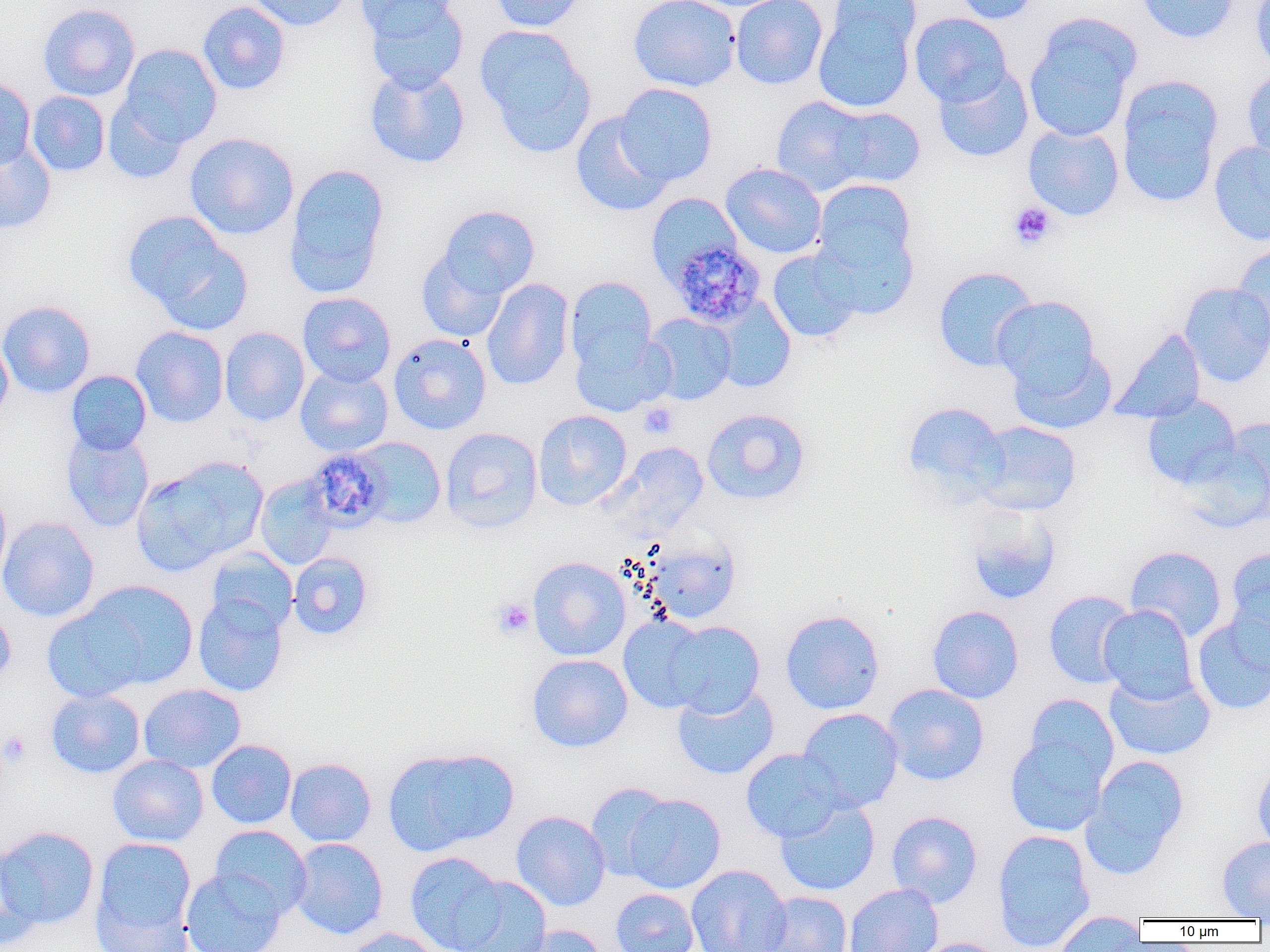

Approximate bounding boxes as (x1, y1, x2, y2) in pixels. Platelet locations: (1008, 202, 1056, 250), (639, 402, 678, 439), (491, 597, 536, 639), (0, 730, 32, 767). Plasmodium malariae-infected red blood cell locations: (668, 240, 766, 328), (303, 447, 391, 533). Uninfected red blood cell locations: (245, 0, 353, 32), (357, 0, 458, 42), (363, 0, 469, 93), (488, 0, 589, 33), (628, 0, 741, 92), (730, 0, 827, 90), (828, 0, 921, 57), (950, 0, 1042, 24), (1136, 0, 1239, 44), (1249, 0, 1270, 74), (196, 1, 291, 95), (37, 3, 140, 101), (812, 9, 916, 114), (909, 12, 1012, 107), (1023, 14, 1141, 143), (475, 25, 596, 157), (118, 43, 222, 148), (364, 64, 470, 168), (933, 65, 1034, 163), (1241, 70, 1270, 167), (0, 76, 36, 171), (1116, 76, 1223, 207), (614, 83, 718, 186), (27, 91, 109, 177), (102, 95, 191, 185), (771, 96, 873, 195), (827, 105, 926, 189), (570, 113, 673, 217), (1023, 124, 1124, 221), (184, 132, 299, 240), (0, 141, 56, 235), (1208, 141, 1270, 246), (720, 162, 827, 259), (283, 163, 390, 298), (812, 179, 916, 272), (646, 193, 742, 286), (436, 205, 540, 300), (123, 212, 247, 328), (813, 226, 919, 320), (1232, 243, 1270, 347), (416, 248, 510, 343), (767, 248, 862, 342), (932, 266, 1039, 372), (565, 276, 658, 372), (481, 278, 574, 391), (1179, 282, 1270, 387), (297, 292, 396, 387), (707, 295, 796, 393), (992, 295, 1100, 391), (0, 300, 96, 398), (644, 313, 737, 405), (131, 326, 229, 427), (219, 327, 310, 426), (1110, 327, 1207, 425), (570, 328, 675, 417), (0, 332, 14, 422), (388, 333, 492, 435), (1008, 345, 1117, 435), (295, 365, 393, 457), (65, 370, 152, 456), (1142, 394, 1241, 489), (903, 401, 1009, 502), (701, 407, 810, 505), (533, 409, 632, 510), (1221, 417, 1270, 505), (971, 420, 1082, 516), (60, 427, 154, 533), (439, 427, 542, 534), (351, 437, 446, 529), (1178, 440, 1270, 534), (612, 442, 710, 532), (131, 456, 268, 576), (254, 475, 339, 571), (0, 485, 11, 588), (964, 505, 1061, 606), (0, 516, 99, 622), (645, 537, 740, 624), (1225, 545, 1270, 655), (1124, 546, 1227, 641), (205, 547, 298, 635), (288, 552, 373, 641), (527, 556, 631, 661), (77, 580, 198, 690), (1043, 590, 1137, 688), (193, 594, 289, 697), (0, 602, 16, 687), (1098, 604, 1199, 704), (42, 605, 148, 703), (927, 605, 1024, 704), (780, 609, 885, 715), (618, 615, 714, 714), (1190, 616, 1270, 715), (665, 620, 765, 717), (526, 654, 633, 752), (1104, 671, 1215, 761), (138, 683, 246, 773), (882, 683, 989, 786), (672, 685, 779, 780), (45, 689, 146, 778), (1022, 693, 1119, 786), (797, 708, 904, 813), (1004, 732, 1111, 837), (206, 739, 297, 829), (383, 746, 519, 856), (740, 749, 846, 842), (107, 754, 209, 847), (1082, 754, 1190, 876), (285, 758, 376, 847), (1251, 760, 1270, 854), (585, 782, 675, 881), (621, 792, 726, 894), (775, 800, 880, 896), (511, 810, 610, 911), (886, 810, 983, 908), (210, 825, 312, 919), (0, 826, 100, 930), (992, 829, 1096, 952), (1216, 836, 1270, 920), (91, 837, 197, 949), (289, 837, 389, 940), (0, 847, 43, 951), (404, 851, 508, 952), (686, 864, 791, 952), (181, 866, 286, 952), (453, 876, 552, 952), (844, 883, 944, 952), (610, 888, 699, 952), (760, 890, 853, 952), (1052, 911, 1146, 950), (508, 925, 607, 952), (339, 927, 444, 952), (909, 937, 1007, 952). Slide-level diagnosis: Plasmodium malariae. Image is 1270×952 pixels. 1000x magnification. One field of a larger specimen. Thin blood smear. Light microscopy.